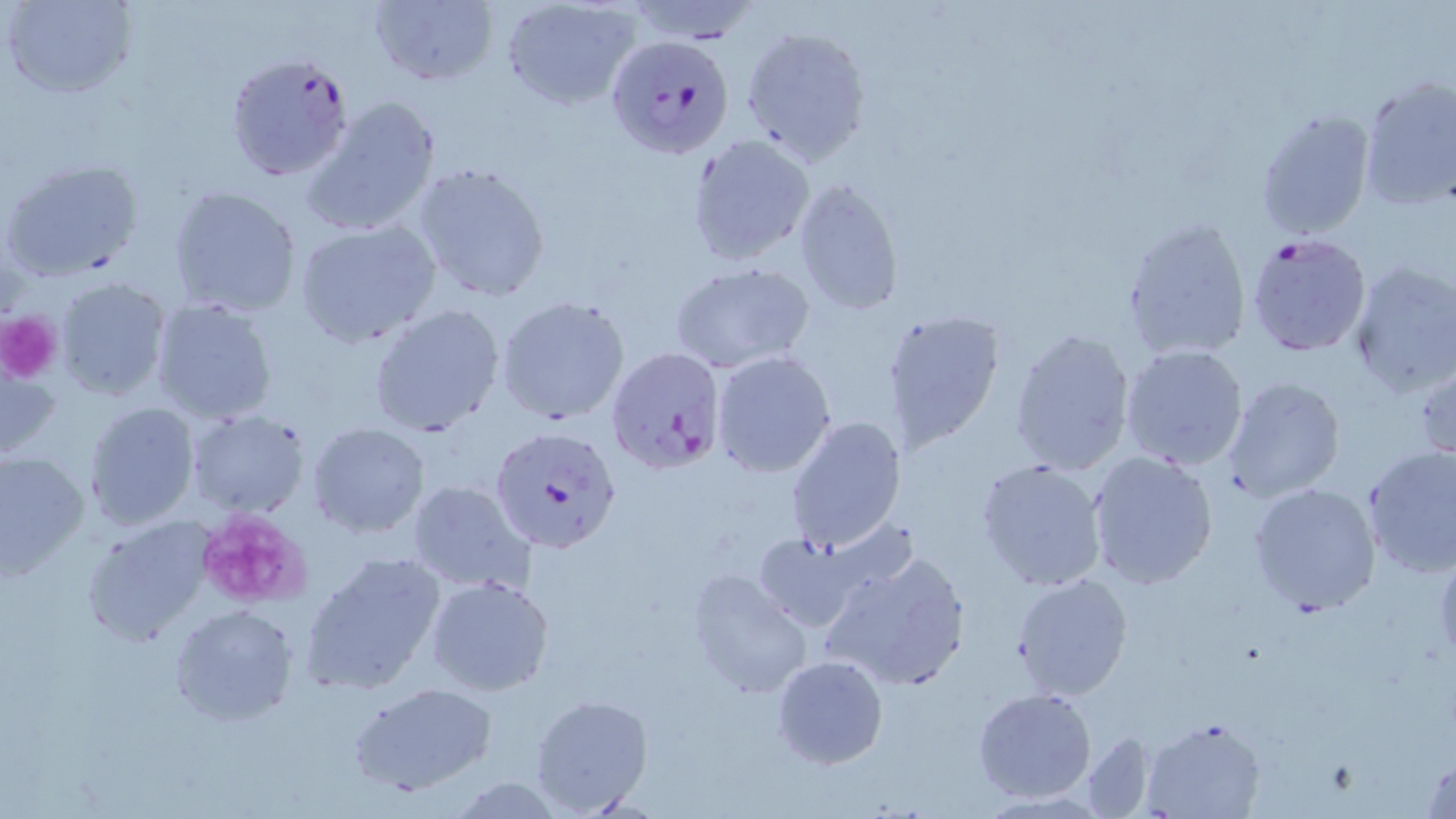
Approximate bounding boxes as (x1, y1, x2, y2) in pixels. Uninfected red blood cell locations: (2, 0, 137, 100), (368, 0, 498, 88), (502, 2, 640, 110), (742, 23, 874, 164), (1357, 77, 1456, 210), (302, 94, 443, 237), (1255, 106, 1376, 240), (687, 134, 815, 267), (2, 157, 144, 284), (410, 161, 553, 302), (794, 178, 905, 317), (169, 186, 302, 318), (1121, 215, 1252, 363), (293, 220, 441, 348), (1346, 259, 1456, 398), (669, 262, 815, 374), (56, 277, 171, 401), (496, 295, 631, 426), (150, 299, 278, 425), (369, 304, 506, 438), (878, 308, 1005, 450), (1009, 326, 1138, 476), (1118, 343, 1250, 471), (711, 350, 836, 477), (1415, 361, 1456, 468), (1, 364, 59, 464), (1222, 377, 1346, 502), (83, 401, 200, 530), (185, 409, 310, 519), (786, 416, 907, 552), (306, 421, 431, 538), (1362, 445, 1456, 578), (1085, 449, 1220, 590), (0, 450, 90, 579), (975, 458, 1109, 592), (405, 480, 536, 597), (1248, 481, 1381, 615), (81, 518, 213, 644), (751, 530, 873, 633), (817, 549, 972, 694), (300, 551, 448, 695), (685, 566, 812, 699), (1011, 572, 1135, 702), (425, 575, 556, 698), (169, 602, 302, 726), (771, 654, 887, 769), (348, 681, 499, 797), (972, 687, 1095, 804), (530, 693, 654, 817), (1143, 717, 1266, 819), (1079, 730, 1160, 817), (1420, 755, 1455, 817), (448, 777, 565, 817). Platelet locations: (0, 310, 63, 384), (194, 509, 312, 609). Plasmodium falciparum-infected red blood cell locations: (609, 37, 738, 163), (224, 51, 355, 181), (1243, 230, 1373, 358), (607, 347, 727, 474), (490, 425, 622, 554). Slide-level diagnosis: Plasmodium falciparum. May-Grünwald-Giemsa-stained preparation. 1000x magnification. Thin blood smear. Optical microscopy. Image is 1456×819 pixels. Single field of view.